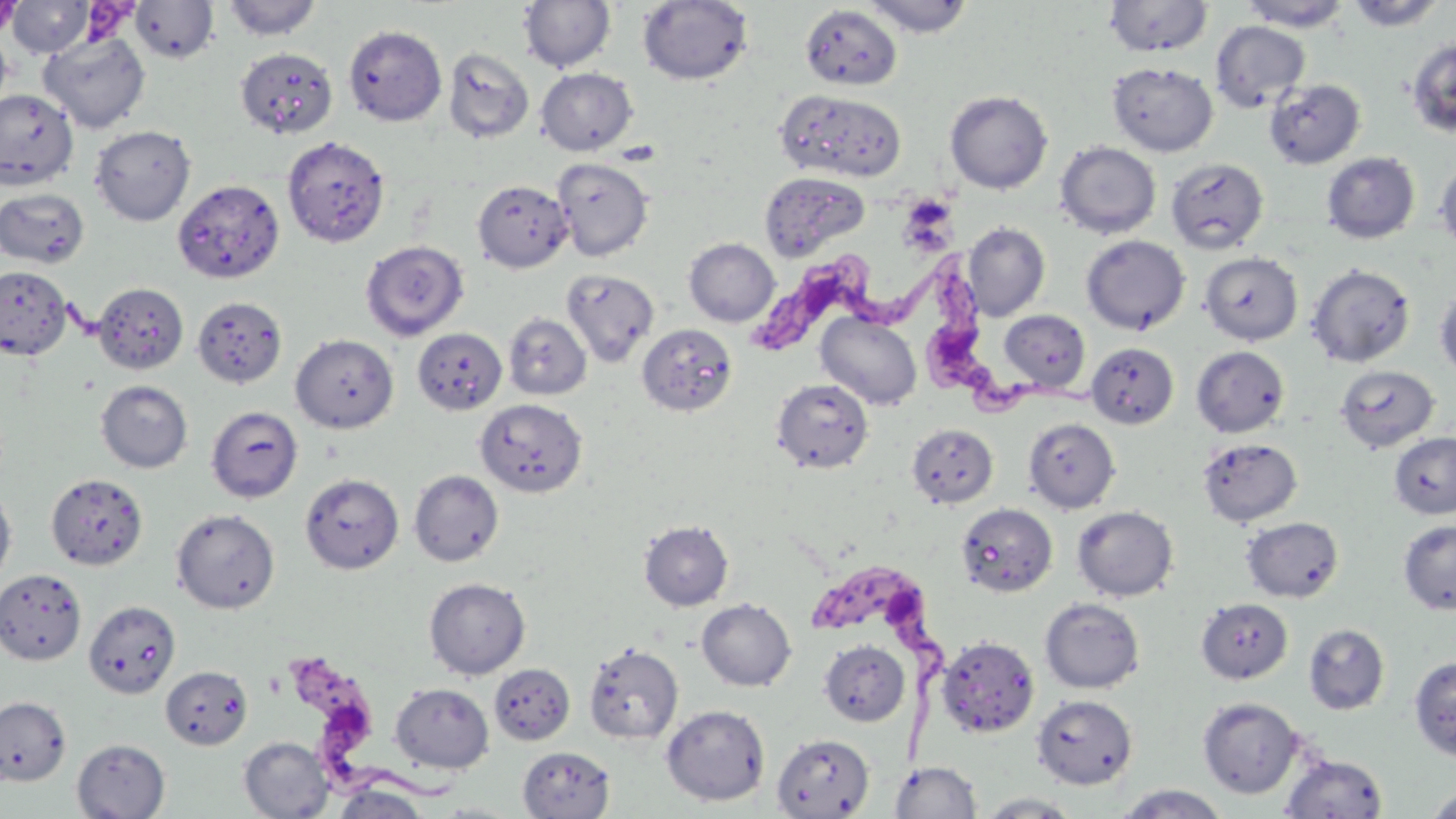
Trypanosoma brucei locations = approximate bounding boxes as (x1,y1)-(x2,y2) corner pairs in pixels: (913,238)-(1093,427), (745,257)-(953,338), (808,560)-(957,778), (283,651)-(464,804)
slide-level diagnosis = Trypanosoma brucei
image size = 1456×819 pixels
magnification = 1000x
preparation = thin blood smear
uninfected red blood cell locations = approximate bounding boxes as (x1,y1)-(x2,y2) corner pairs in pixels: (0,0)-(23,37), (7,0)-(92,58), (221,0)-(323,42), (637,0)-(754,86), (860,0)-(976,38), (1103,0)-(1213,57), (1343,0)-(1448,32), (519,1)-(616,72), (1238,1)-(1352,31), (130,2)-(220,64), (800,4)-(902,91), (1211,21)-(1310,112), (343,24)-(447,126), (0,29)-(13,113), (39,31)-(151,133), (1405,35)-(1456,139), (235,47)-(338,139), (442,47)-(534,144), (1107,62)-(1218,157), (535,67)-(637,155), (1264,78)-(1365,168), (944,89)-(1053,194), (0,90)-(78,188), (775,90)-(907,183), (90,125)-(196,225), (281,135)-(390,248), (1054,141)-(1161,239), (1321,152)-(1420,244), (552,158)-(654,261), (1166,158)-(1269,254), (1434,158)-(1456,256), (758,171)-(870,259), (172,179)-(285,284), (472,179)-(572,273), (0,187)-(90,268), (963,222)-(1050,320), (1081,235)-(1190,335), (684,238)-(779,327), (360,240)-(469,341), (1199,251)-(1302,345), (1306,264)-(1416,368), (0,266)-(73,360), (560,269)-(659,366), (93,282)-(188,375), (1435,287)-(1456,382), (193,296)-(287,388), (999,310)-(1090,392), (816,312)-(922,410), (503,313)-(592,400), (637,323)-(737,416), (412,327)-(507,415), (291,334)-(399,433), (1086,342)-(1179,429), (1191,345)-(1290,437), (1334,364)-(1440,453), (771,378)-(874,473), (95,380)-(193,472), (475,398)-(588,497), (206,406)-(303,502), (1024,417)-(1120,514), (906,423)-(998,507), (1388,432)-(1456,520), (1197,437)-(1302,526), (408,470)-(504,566), (300,472)-(404,573), (46,473)-(148,570), (0,485)-(17,589), (955,503)-(1058,598), (1072,505)-(1178,602), (171,508)-(280,614), (1241,516)-(1345,602), (638,519)-(734,611), (1398,519)-(1456,615), (0,569)-(86,666), (424,577)-(530,679), (1039,597)-(1145,694), (696,598)-(796,691), (1195,598)-(1294,684), (83,601)-(180,698), (1303,623)-(1390,715), (936,635)-(1039,737), (819,640)-(909,727), (583,642)-(684,745), (1409,655)-(1456,762), (490,663)-(575,745), (160,665)-(253,749), (390,682)-(494,773), (1032,694)-(1137,790), (0,696)-(71,785), (1197,696)-(1304,799), (661,704)-(770,806), (772,733)-(875,818), (239,736)-(334,818), (72,739)-(170,818), (518,746)-(615,819), (1280,753)-(1388,818), (889,761)-(982,818), (330,783)-(432,819), (1112,784)-(1233,818), (1423,784)-(1456,819), (973,792)-(1085,818), (425,801)-(527,818)
modality = light microscopy
field of view = one of a larger specimen
stain = May-Grünwald-Giemsa